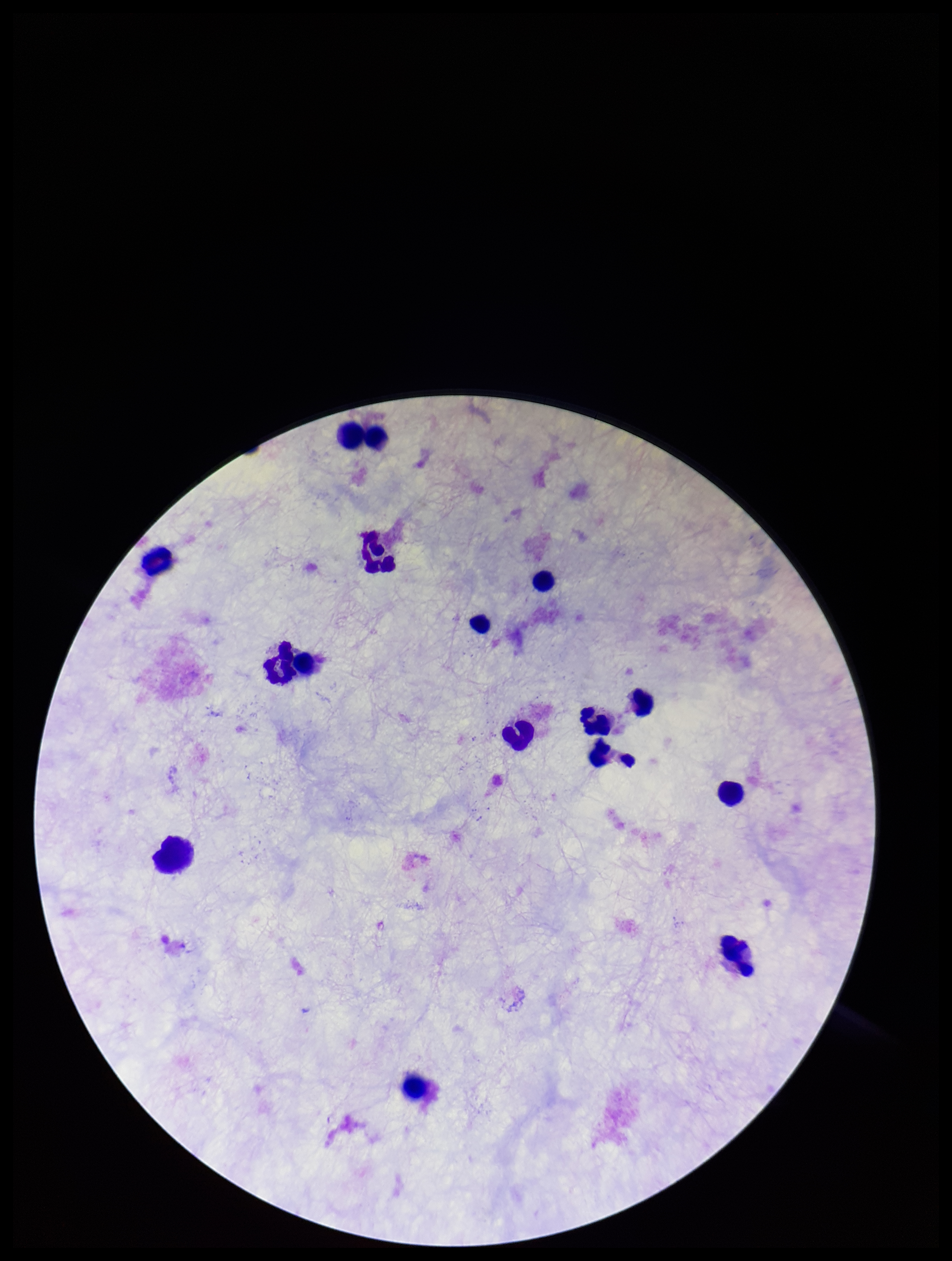
Summary:
  - Leukocyte count: 14
  - Parasite count: 0
  - Image size: 952×1261 pixels
  - Plasmodium parasites: none detected
  - Capture: smartphone photograph through the microscope eyepiece
  - Field of view: single
  - Patient malaria status: negative
  - Stain: Giemsa
  - Preparation: thick